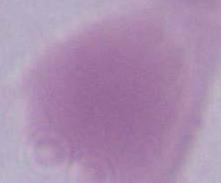
magnification = 1000x
modality = photomicrograph
identification = red blood cell